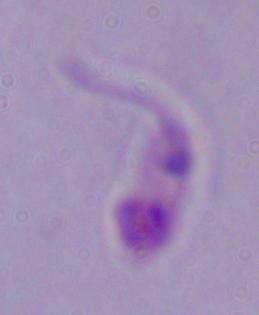 Micrograph. A Leishmania parasite is seen. 1000x magnification.